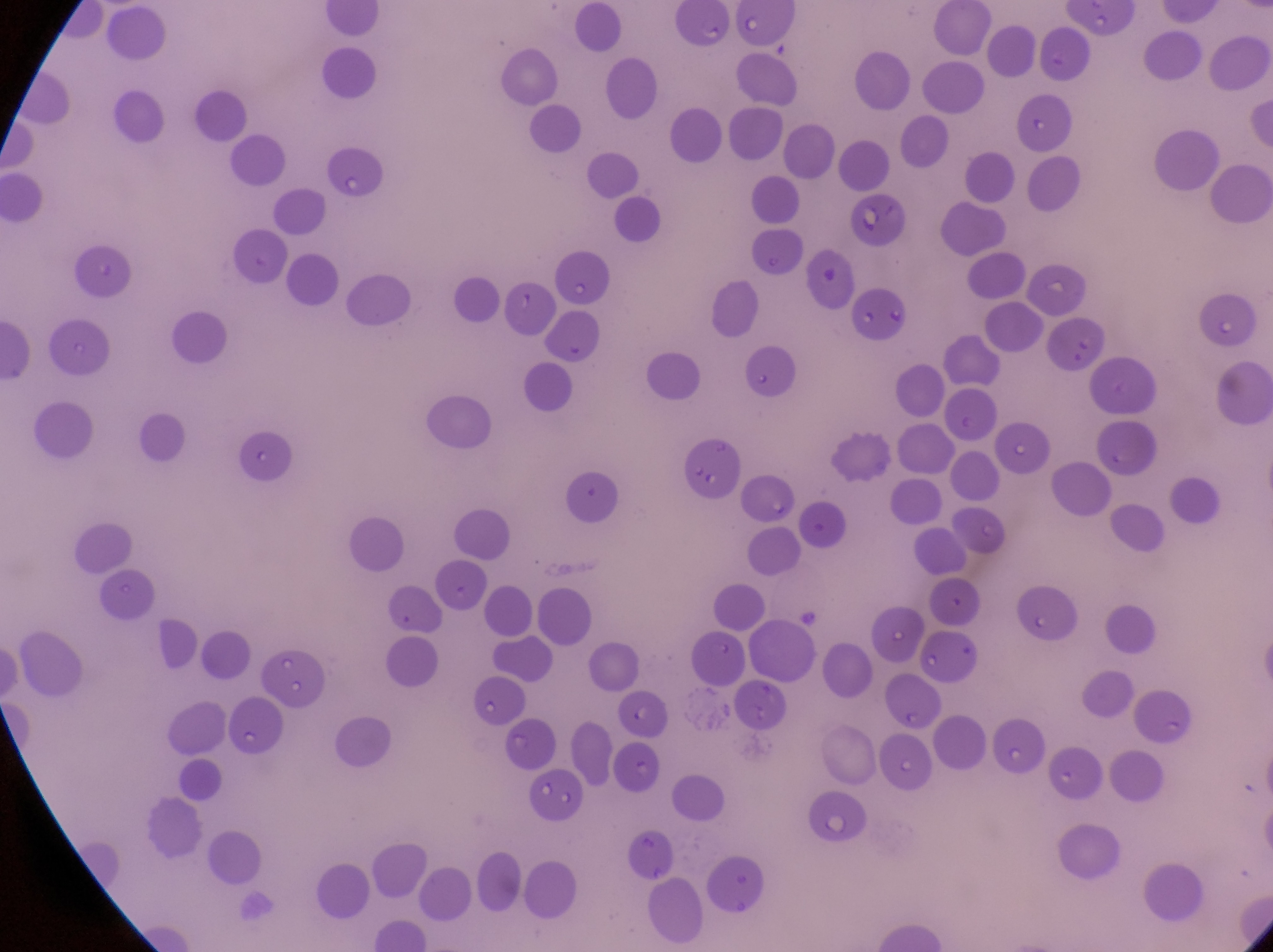
Approximate bounding boxes as {left, top, right, bottom} in pixels.
Summary:
  - Parasitised red blood cell locations: {662, 2, 729, 52}, {317, 143, 380, 200}, {838, 199, 912, 256}
  - Country: Uganda
  - Image size: 1273×952 pixels
  - Capture: smartphone photograph through the eyepiece of an Olympus CX-23 microscope
  - Field of view: single
  - Magnification: 1000x
  - Preparation: thin blood film